Name the parasite shown.
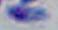

This is Toxoplasma gondii.

Captured at 1000x magnification. Photomicrograph.